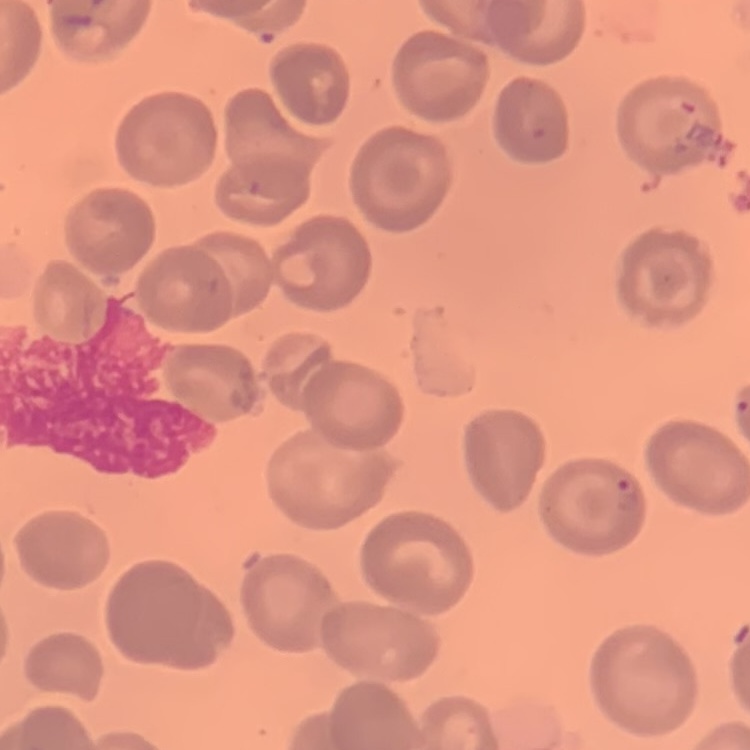
{
  "erythrocyte_morphology": "no rouleaux formation",
  "stain": "Field's or Giemsa",
  "image_type": "one tile cut from a larger photomicrograph",
  "preparation": "thin blood film"
}